Outline each P. falciparum parasite and classify it by life-cycle stage.
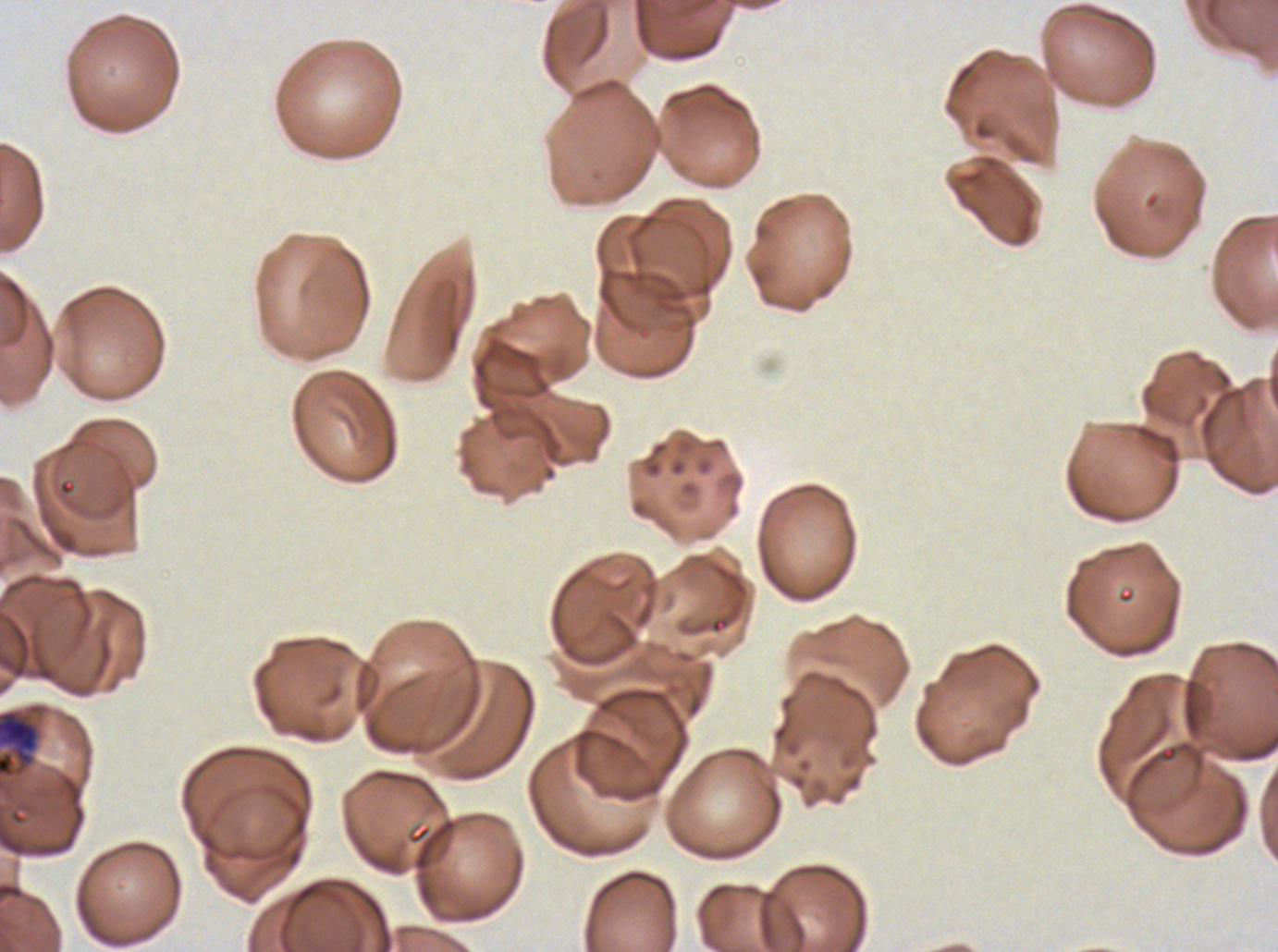

Approximate bounding boxes as [x1, y1, x2, y2] in pixels.
Late trophozoites: [0, 708, 41, 779].
No rings, late-ring/early-trophozoite forms, mid trophozoites, early schizonts, late schizonts, segmenters, or gametocytes observed.

Summary:
  - Image size: 1278×952 pixels
  - Preparation: thin blood smear
  - Specimen: ex-vivo P. falciparum culture from a patient in The Gambia, grown for 24 to 48 hours
  - Stain: Giemsa
  - Field of view: sub-image separated from a larger composite